Name the cell type shown.
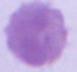

This is an erythrocyte.

Summary:
  - Magnification: 1000x
  - Modality: micrograph